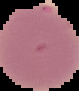
Summary:
  - Image size: 79×91 pixels
  - Malaria status: uninfected
  - Preparation: thin blood smear
  - Image type: cell region segmented out of the field of view; surrounding area masked to black